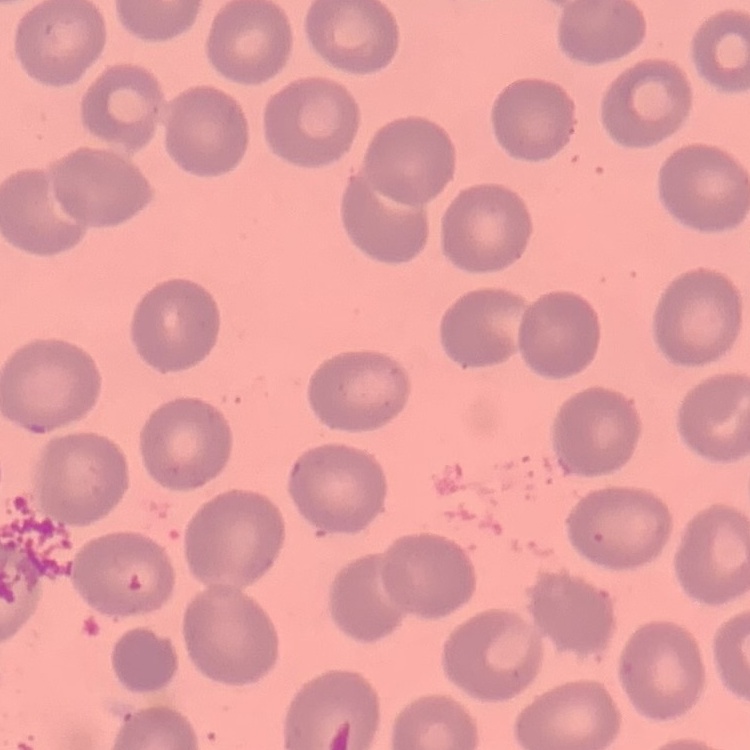

red blood cell morphology = no rouleaux formation
stain = Field's or Giemsa
image type = square crop of a larger photomicrograph
preparation = thin blood film